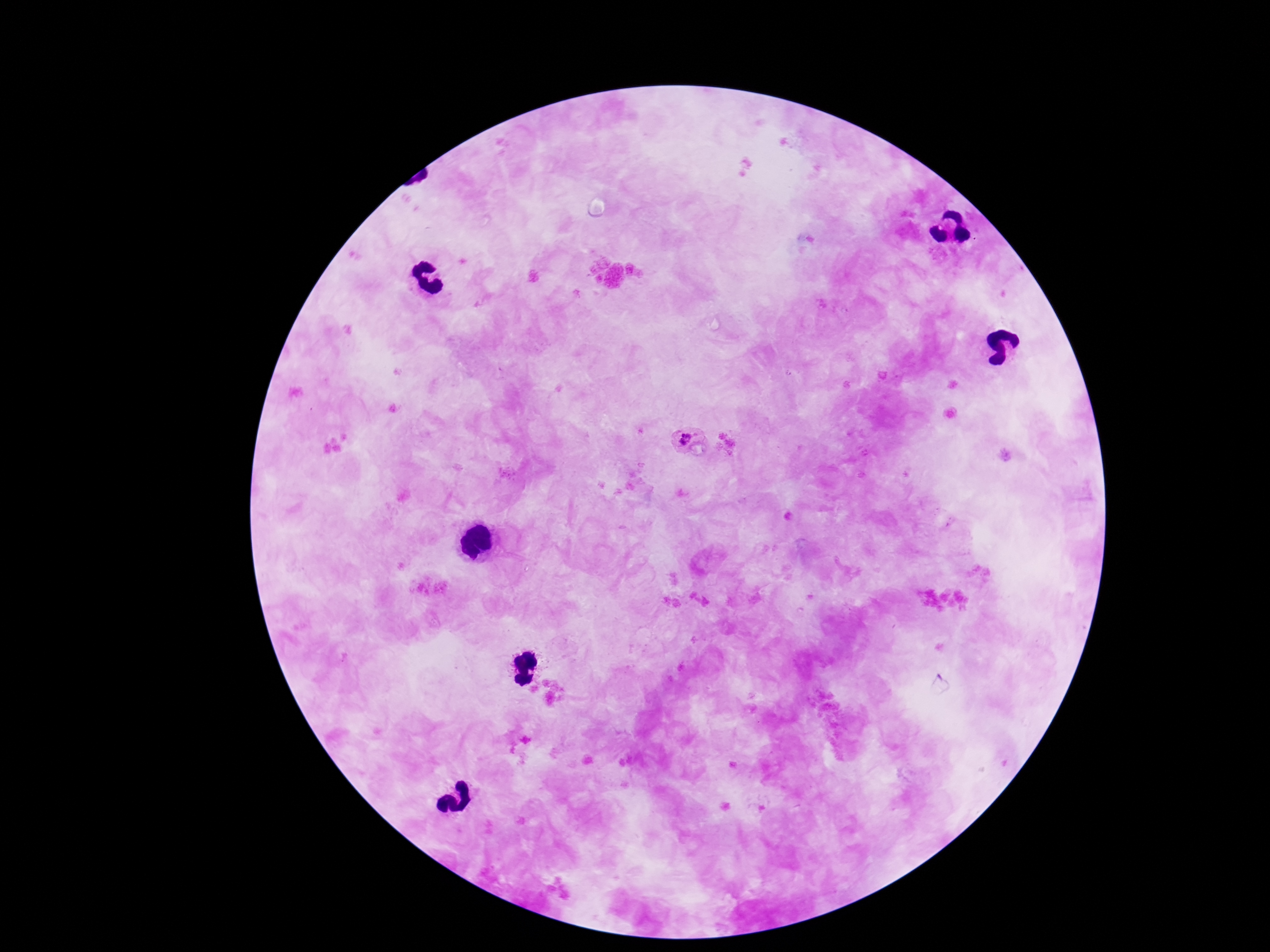
Approximate centers as {x, y} in pixels. Plasmodium parasite locations: {685, 441}. Patient malaria status: positive. Photographed through the microscope eyepiece with a smartphone camera. Single field of view. Giemsa stain. Image is 1270×952 pixels. 100x magnification. Thick blood film.